Locate every Plasmodium malariae-infected red blood cell.
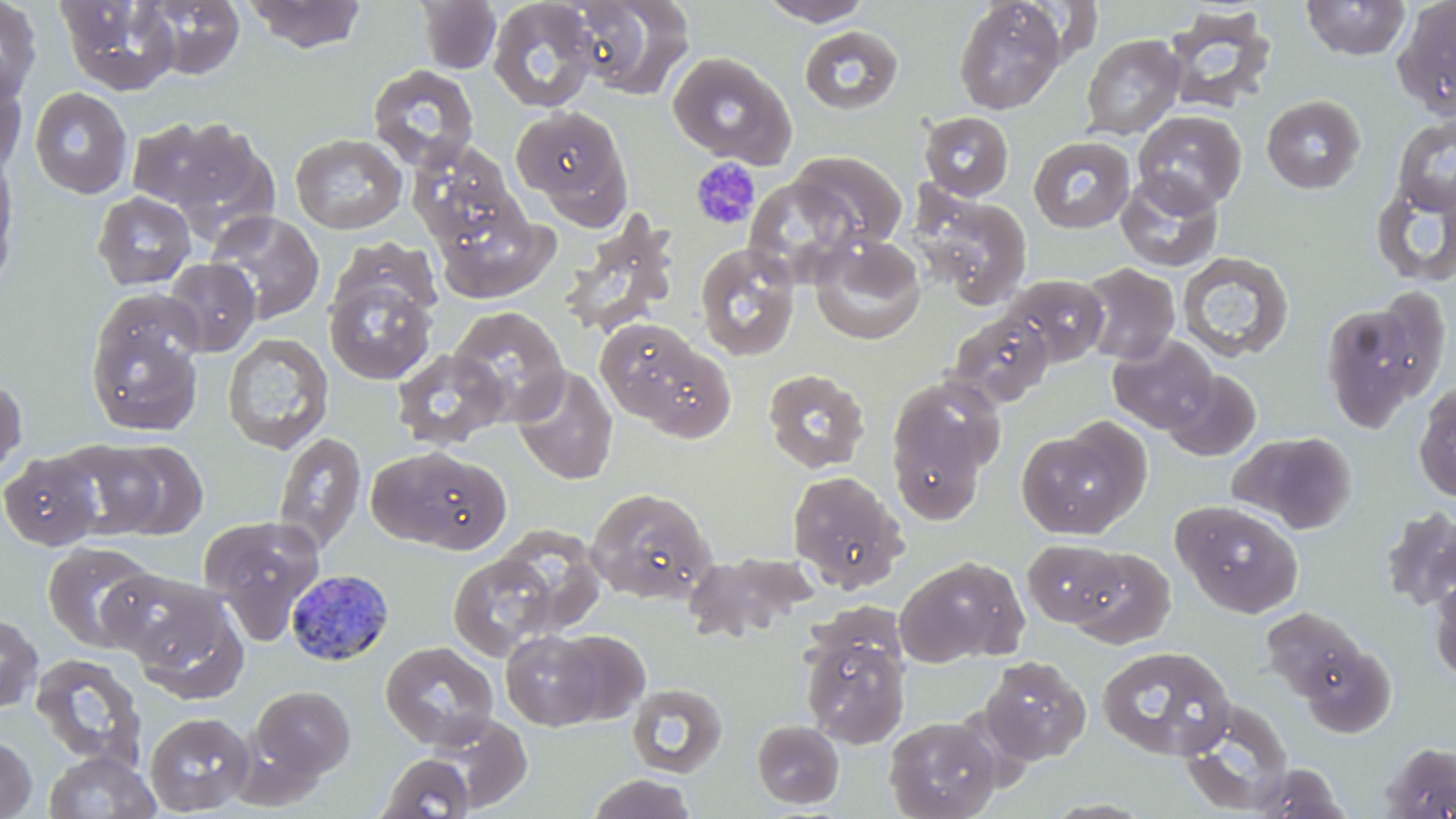
Approximate bounding boxes as (x1,y1)-(x2,y2) corner pairs in pixels.
Plasmodium malariae-infected red blood cells: (286,569)-(394,666).

slide-level diagnosis = Plasmodium malariae
stain = May-Grünwald-Giemsa
uninfected red blood cell locations = approximate bounding boxes as (x1,y1)-(x2,y2) corner pairs in pixels: (0,0)-(42,104), (241,0)-(368,53), (417,0)-(502,74), (566,0)-(696,100), (756,0)-(876,26), (1392,0)-(1456,120), (55,1)-(182,95), (142,1)-(245,80), (487,1)-(600,112), (953,1)-(1066,114), (1301,1)-(1411,60), (1163,8)-(1277,114), (798,25)-(904,115), (1080,33)-(1186,140), (667,51)-(795,166), (0,64)-(28,175), (368,64)-(480,171), (29,87)-(134,199), (1261,95)-(1366,194), (509,106)-(632,221), (1132,110)-(1247,213), (919,112)-(1014,200), (1392,113)-(1456,216), (127,115)-(235,211), (169,123)-(280,241), (290,133)-(408,234), (1028,135)-(1135,234), (409,142)-(526,253), (789,151)-(908,251), (0,153)-(22,294), (1115,171)-(1224,273), (745,178)-(860,286), (1370,178)-(1456,289), (913,188)-(1033,309), (92,191)-(196,290), (433,198)-(558,303), (205,211)-(325,324), (808,235)-(926,345), (694,242)-(801,361), (1177,251)-(1295,363), (162,258)-(260,356), (1078,263)-(1180,365), (324,271)-(438,385), (1002,274)-(1109,368), (85,292)-(208,438), (1319,297)-(1439,432), (448,306)-(570,425), (946,311)-(1055,409), (606,328)-(737,442), (222,332)-(334,455), (1107,334)-(1219,434), (391,347)-(510,450), (511,366)-(619,485), (762,368)-(870,473), (1162,369)-(1261,461), (884,376)-(1002,526), (0,378)-(27,480), (1413,380)-(1456,504), (1015,426)-(1142,538), (1231,430)-(1356,533), (274,432)-(366,555), (98,440)-(208,539), (57,441)-(166,540), (367,446)-(507,551), (0,451)-(103,551), (786,470)-(908,593), (581,486)-(718,605), (1173,500)-(1304,617), (1379,506)-(1456,612), (198,515)-(326,640), (494,525)-(607,638), (1021,539)-(1123,628), (42,541)-(158,653), (1069,547)-(1175,648), (686,552)-(824,636), (448,553)-(556,660), (895,555)-(1027,667), (99,568)-(228,670), (1428,576)-(1456,683), (125,587)-(250,704), (1261,607)-(1369,706), (0,613)-(42,712), (501,629)-(606,730), (550,629)-(650,724), (801,631)-(910,750), (380,641)-(499,750), (1296,641)-(1397,738), (1097,645)-(1235,761), (30,651)-(148,768), (979,656)-(1092,765), (626,683)-(727,777), (251,685)-(356,782), (1178,698)-(1294,815), (144,712)-(255,815), (425,714)-(533,811), (884,716)-(1000,819), (752,719)-(844,809), (0,734)-(37,818), (1379,741)-(1456,818), (43,750)-(161,819), (376,753)-(475,818), (1251,762)-(1350,819), (586,773)-(697,818)
modality = light microscopy
magnification = 1000x
preparation = thin blood film
field of view = single
platelet locations = approximate bounding boxes as (x1,y1)-(x2,y2) corner pairs in pixels: (689,158)-(761,232)
image size = 1456×819 pixels